Classify this cell by malaria status.
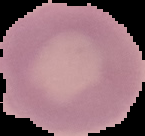

It is uninfected.

From a thin blood film. The area outside the segmented cell region is set to black. Image is 145×136 pixels.